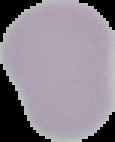 Result: no Plasmodium parasites seen. Image is 115×142 pixels. Segmented cell region on a black background. From a thin blood film.